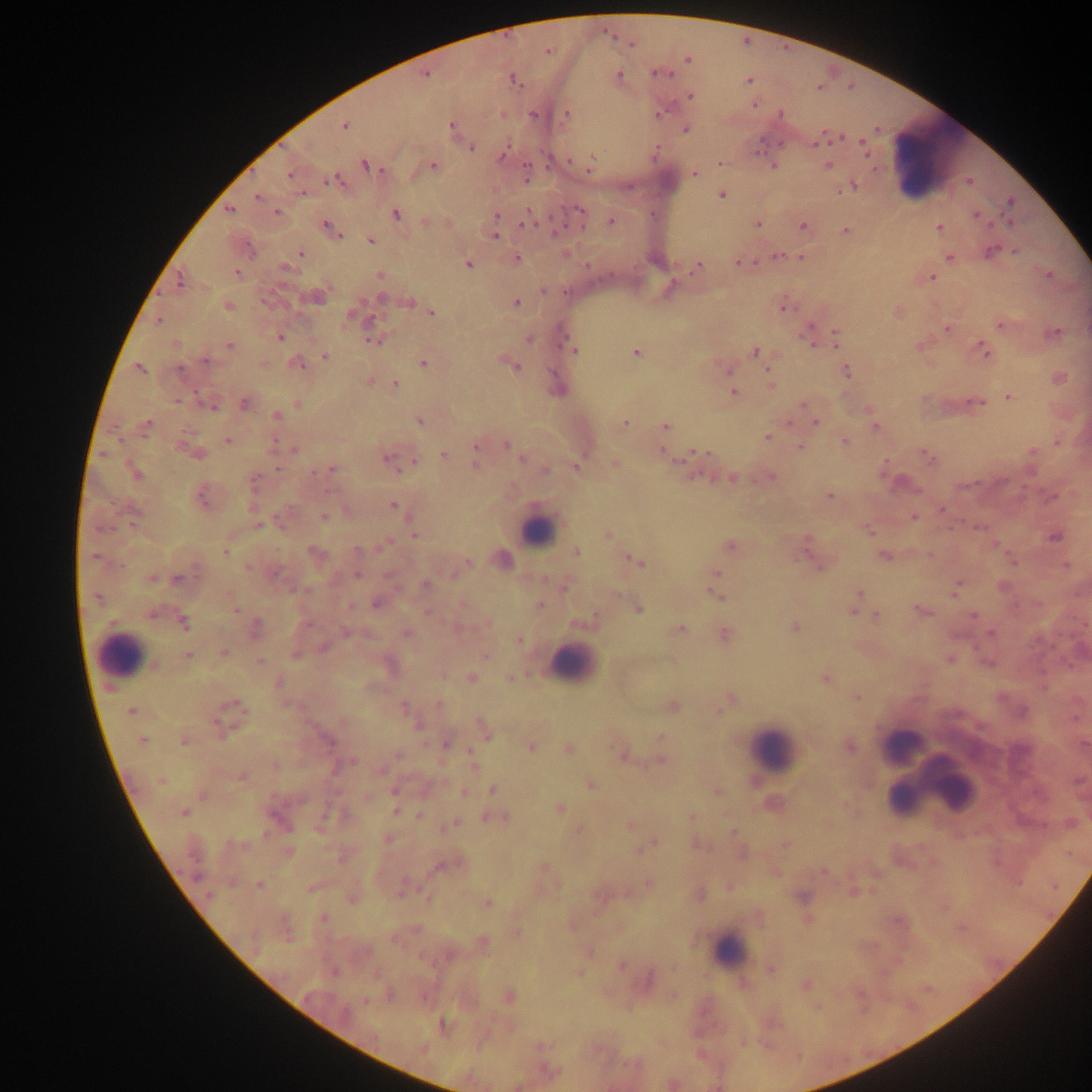
Approximate centers as x y in pixels.
Summary:
  - Malaria parasite locations: 632 43; 547 51; 688 59; 662 74; 425 75; 619 75; 514 81; 748 81; 691 96; 754 104; 659 114; 781 114; 533 115; 567 115; 452 125; 344 126; 686 129; 838 138; 818 142; 471 148; 864 148; 502 155; 592 163; 719 163; 365 165; 433 165; 828 165; 773 166; 590 169; 526 172; 695 174; 289 175; 334 180; 850 186; 722 195; 257 197; 1010 202; 579 210; 229 211; 277 212; 396 214; 976 214; 497 216; 527 220; 611 222; 757 225; 328 226; 803 226; 939 227; 332 230; 845 230; 495 236; 370 240; 990 252; 1016 252; 301 253; 779 255; 517 258; 801 258; 950 259; 738 262; 468 264; 697 267; 285 268; 238 273; 380 274; 1049 275; 931 278; 179 280; 264 301; 410 302; 517 303; 229 306; 784 308; 432 313; 349 317; 159 320; 1002 325; 947 328; 808 331; 1055 334; 279 336; 836 338; 529 339; 374 341; 229 346; 573 350; 985 350; 756 351; 636 353; 325 356; 207 361; 298 363; 423 363; 515 367; 140 369; 179 370; 767 370; 728 371; 846 371; 395 385; 733 392; 1009 396; 178 401; 245 403; 298 403; 976 403; 802 404; 210 406; 276 415; 420 421; 625 423; 816 423; 148 424; 665 426; 875 427; 767 437; 227 441; 845 443; 1057 443; 506 445; 476 447; 800 447; 294 449; 662 451; 192 452; 700 452; 517 454; 443 455; 927 456; 388 459; 522 459; 415 461; 475 464; 615 465; 577 466; 277 469; 330 470; 546 470; 135 473; 771 477; 732 478; 254 483; 965 485; 829 496; 1053 497; 203 499; 393 506; 942 509; 325 517; 913 517; 258 525; 979 527; 870 531; 608 534; 414 535; 1055 538; 807 540; 382 546; 730 546; 358 549; 225 552; 313 552; 576 552; 883 556; 93 557; 467 561; 636 561; 820 566; 1066 566; 248 567; 277 573; 717 573; 357 575; 152 579; 177 579; 426 584; 1003 587; 955 589; 859 593; 716 594; 97 598; 376 605; 539 605; 350 607; 639 609; 235 610; 921 611; 427 612; 853 612; 973 615; 877 616; 592 618; 184 623; 256 627; 795 628; 680 629; 345 632; 406 634; 990 634; 725 635; 519 640; 323 647; 223 653; 189 656; 295 656; 484 656; 949 659; 260 661; 987 662; 471 677; 509 677; 825 679; 279 683; 856 697; 237 704; 439 704; 403 706; 672 706; 719 710; 131 711; 418 724; 486 731; 660 737; 142 740; 184 741; 328 742; 446 745; 530 746; 850 747; 569 749; 398 754; 621 755; 659 761; 472 762; 275 765; 337 768; 241 778; 160 780; 590 784; 394 790; 493 790; 718 791; 464 793; 203 795; 559 808; 396 811; 184 812; 326 814; 420 815; 498 818; 455 824; 631 825; 579 831; 733 832; 266 834; 389 839; 651 845; 785 845; 341 858; 439 867; 544 867; 647 883; 259 885; 401 893; 700 894; 209 895; 352 899; 429 899; 487 903; 323 918; 517 932; 484 942; 621 966; 771 970; 509 996; 673 996; 366 1001; 443 1024
  - Leukocyte locations: 934 161; 537 530; 120 656; 573 664; 903 744; 772 748; 944 780; 907 791; 901 798; 729 951
  - Capture: mobile-phone photograph through a microscope
  - Preparation: thick blood smear
  - Field of view: single
  - Image size: 1092×1092 pixels
  - Country: Ghana